Identify the parasite.
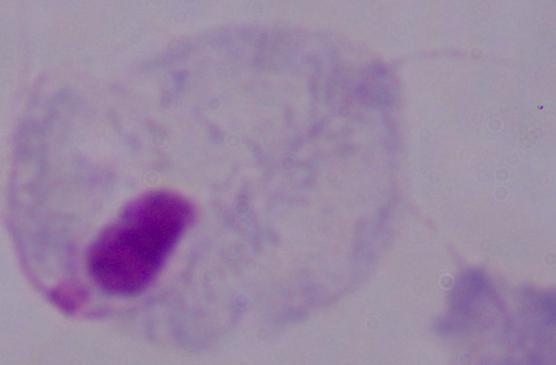
This is a trichomonad.

Captured at 1000x magnification. Photomicrograph.